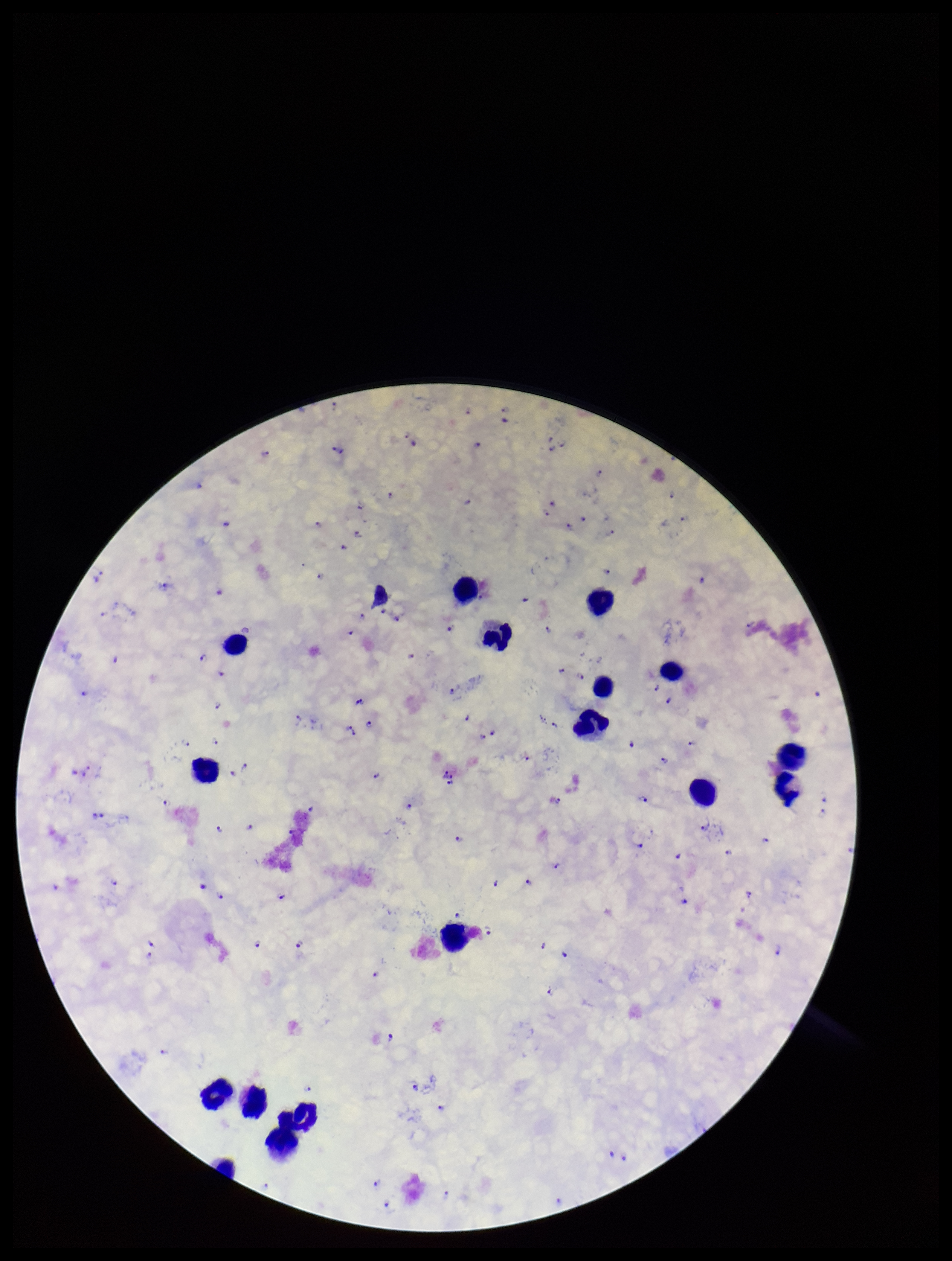
parasite count = 113
patient malaria status = positive
stain = Giemsa
capture = smartphone photograph through the microscope eyepiece
leukocyte count = 17
species reported for this patient = Plasmodium falciparum
Plasmodium parasites = seen
image size = 952×1261 pixels
field of view = one from this slide
preparation = thick